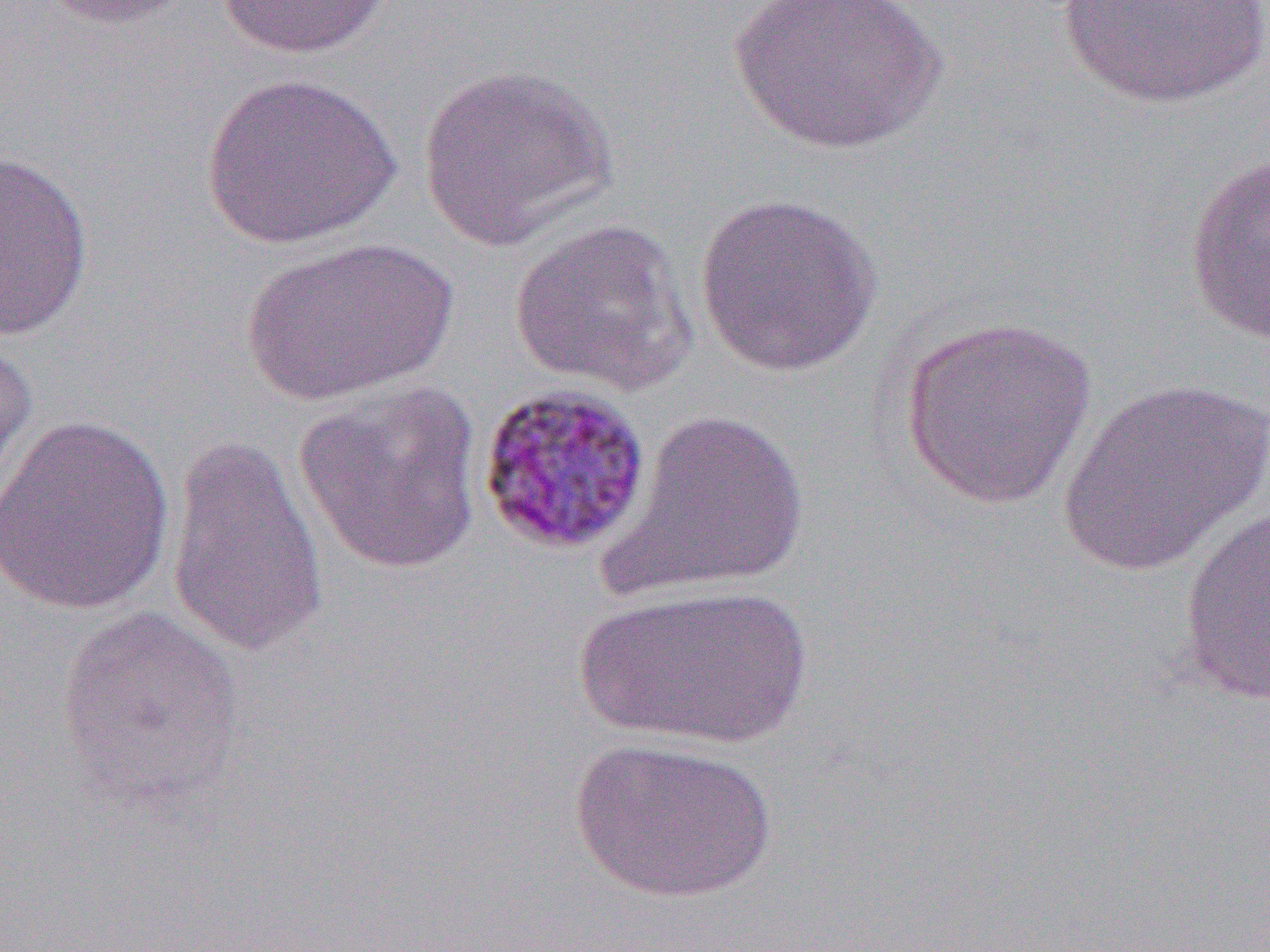

Summary:
  - Coordinate format: approximate bounding boxes as [x1, y1, x2, y2] in pixels
  - Uninfected red blood cell locations: [37, 0, 199, 30], [214, 0, 394, 60], [723, 0, 947, 156], [1050, 0, 1270, 112], [416, 62, 617, 250], [200, 72, 399, 249], [0, 149, 95, 343], [1184, 152, 1270, 348], [694, 192, 883, 378], [507, 216, 699, 396], [240, 235, 456, 407], [898, 314, 1099, 510], [0, 330, 39, 505], [1057, 376, 1270, 575], [292, 382, 484, 577], [605, 406, 811, 601], [1, 414, 176, 616], [164, 434, 329, 659], [1177, 501, 1270, 705], [574, 583, 813, 750], [55, 603, 245, 814], [568, 736, 778, 904]
  - Plasmodium malariae-infected red blood cell locations: [474, 381, 653, 557]
  - Slide-level diagnosis: Plasmodium malariae
  - Modality: optical microscopy
  - Magnification: 1000x
  - Preparation: thin blood smear
  - Field of view: one of a larger specimen
  - Image size: 1270×952 pixels